Report the malaria status of this cell.
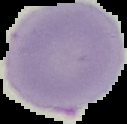
It is uninfected.

From a thin blood film. Image is 127×124 pixels. Cell region segmented out of the field of view; the surrounding area is masked to black.